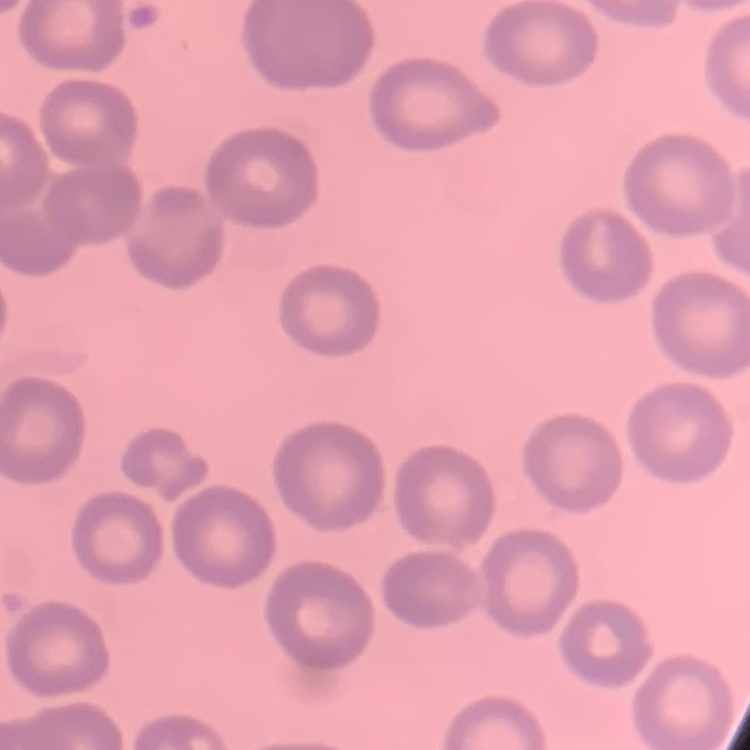

{
  "red_blood_cell_morphology": "no rouleaux formation",
  "image_type": "one tile cut from a larger photomicrograph",
  "preparation": "thin peripheral smear",
  "stain": "Field's or Giemsa"
}